Assess this cell for malaria.
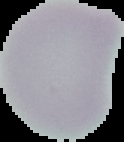
It is uninfected.

preparation = thin blood smear
image size = 124×142 pixels
image type = cell region segmented out of the field of view; surrounding area masked to black